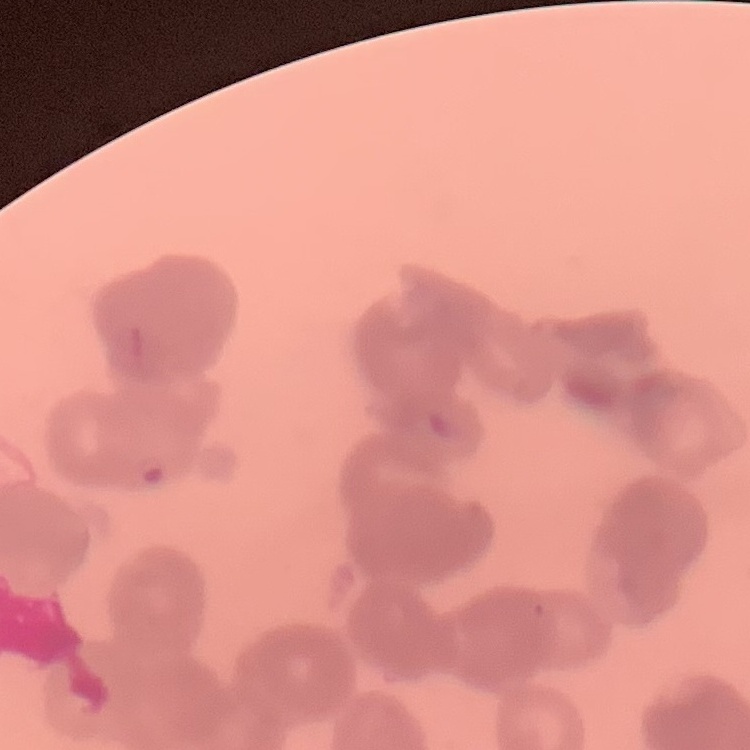
Summary:
  - Erythrocyte morphology: rouleaux formation
  - Stain: Field's or Giemsa
  - Image type: one tile cut from a larger photomicrograph
  - Preparation: thin blood film